Assess this cell for malaria.
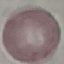

It is uninfected.

Summary:
  - Image type: cell patch, automatically extracted from a larger field of view and resized to 64 × 64 pixels
  - Preparation: thin smear
  - Capture: smartphone through the microscope eyepiece
  - Stain: Giemsa